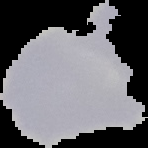

Summary:
  - Preparation: thin blood smear
  - Image type: cell region segmented out of the field of view; surrounding area masked to black
  - Malaria status: uninfected
  - Image size: 148×148 pixels